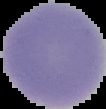

Summary:
  - Image size: 106×109 pixels
  - Result: negative for Plasmodium parasites
  - Image type: segmented cell region with the area outside set to black
  - Preparation: thin blood film